Describe the morphology of the erythrocytes.
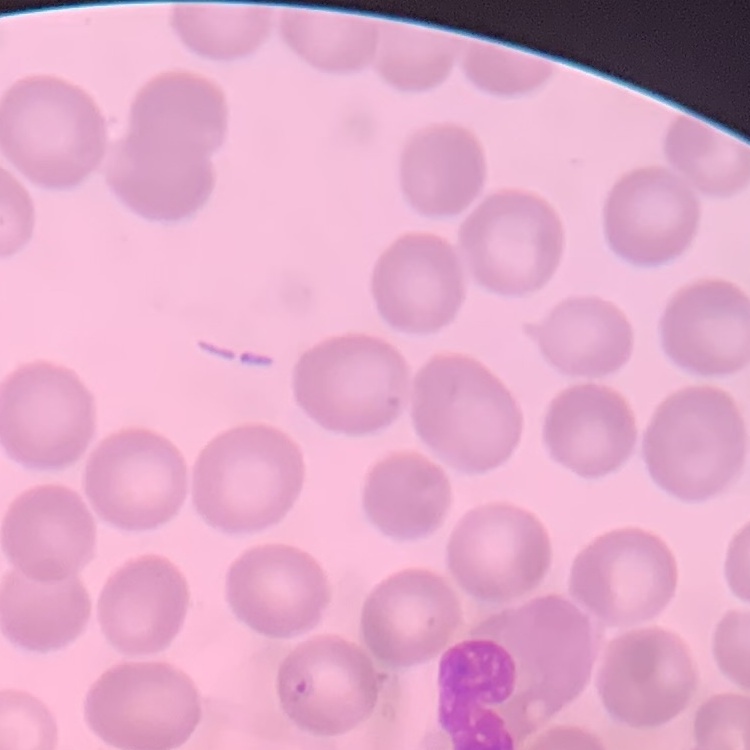
They show no rouleaux formation.

Stained with either Field's or Giemsa. Square crop of a larger photomicrograph. Thin blood smear.